Assess this cell for malaria.
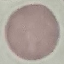

It is uninfected.

Giemsa stain. Photographed with a smartphone camera at the microscope eyepiece. Automatically extracted cell patch, resized to 64 × 64 pixels. Thin blood smear.